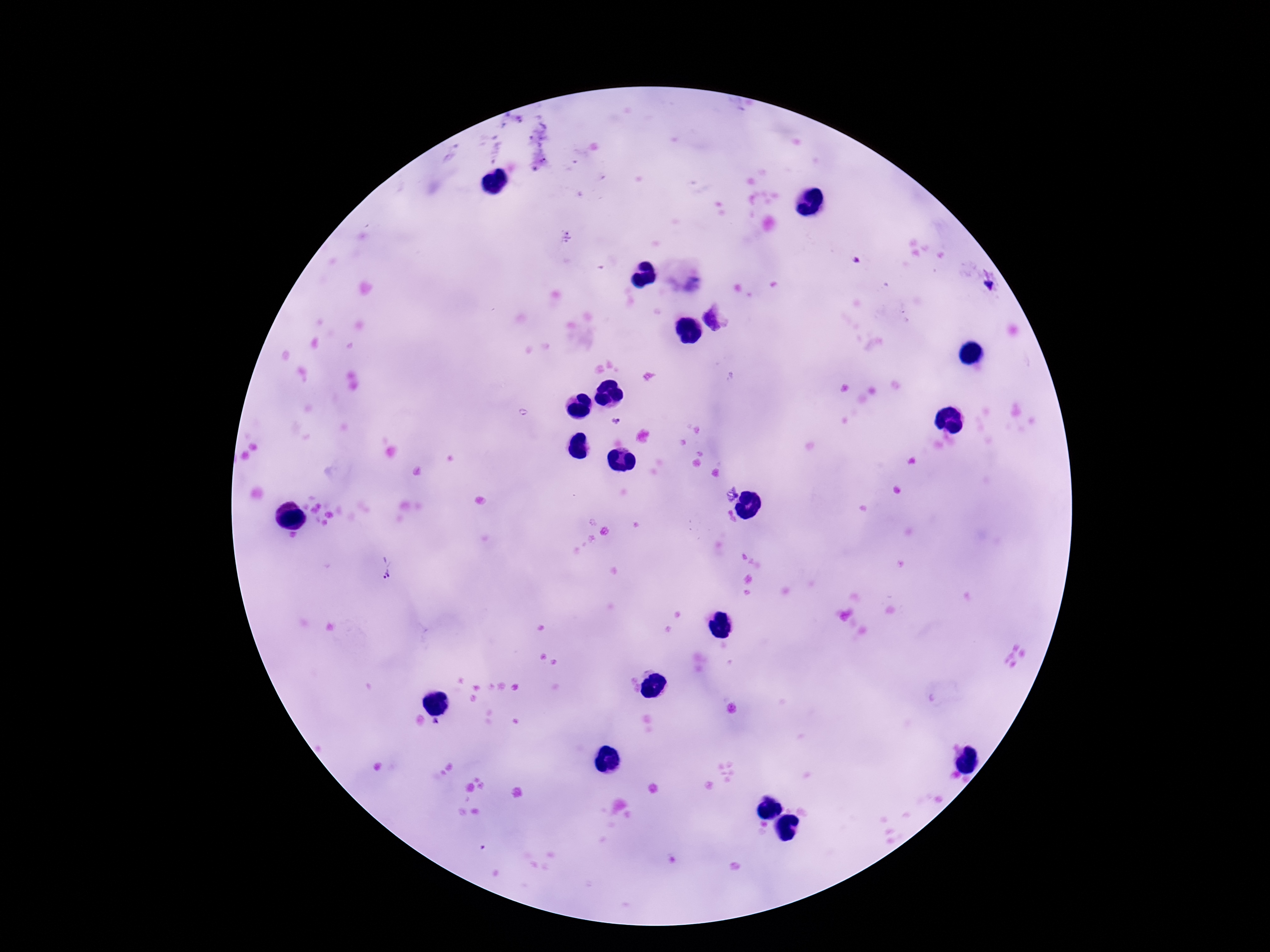

capture: smartphone camera through the microscope eyepiece
field_of_view: single
plasmodium_parasite_locations: 'approximate centers as [x, y] in pixels: [565, 238], [858, 260], [718, 318], [618, 420], [388, 573], [437, 724]'
magnification: 100x
patient_malaria_status: infected
stain: Giemsa
preparation: thick blood smear
image_size: 1270×952 pixels